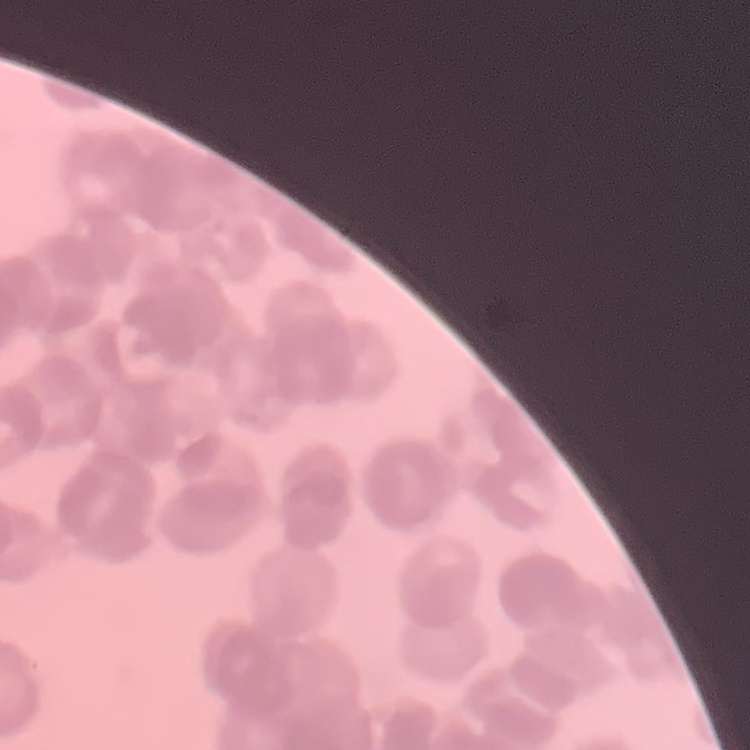

The erythrocytes show rouleaux formation. Thin blood film. Stained with either Field's or Giemsa. Square crop of a larger photomicrograph.